Identify the parasite.
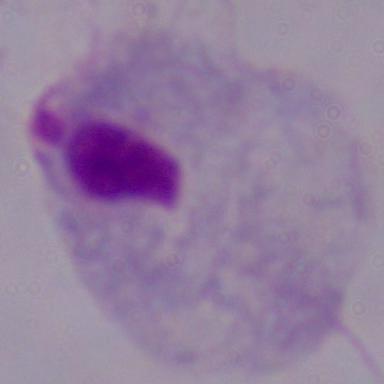
This is a trichomonad.

magnification: 1000x
modality: photomicrograph